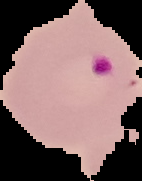
Summary:
  - Preparation: thin blood smear
  - Image type: segmented cell region on a black background
  - Image size: 142×181 pixels
  - Result: malaria parasites detected